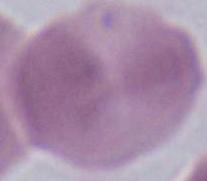

Summary:
  - Modality: photomicrograph
  - Magnification: 1000x
  - Identification: red blood cell